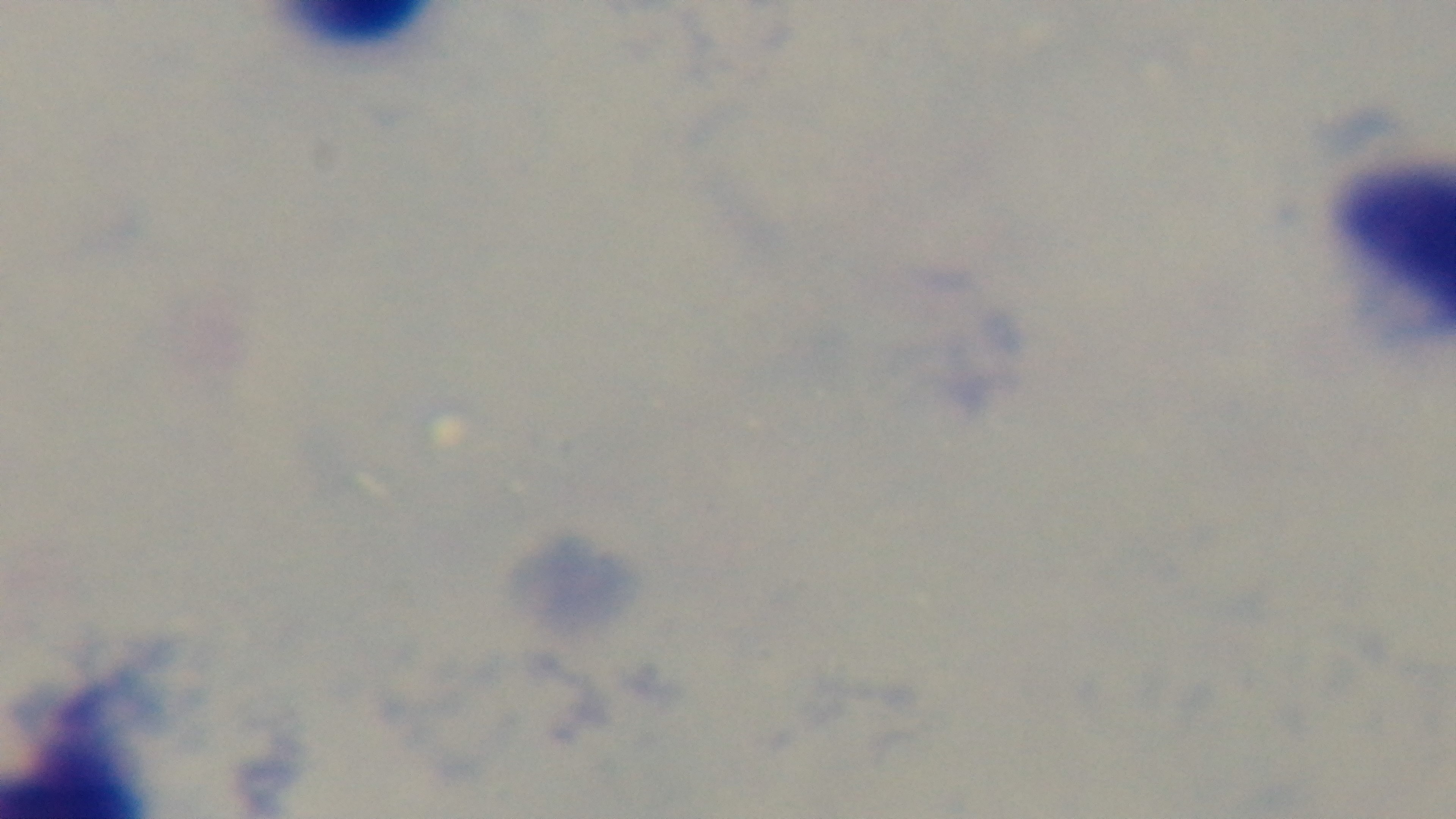

Summary:
  - Malaria status: uninfected
  - Modality: light microscopy
  - Stain: Giemsa
  - Preparation: thick blood film
  - Objective: 100x oil immersion
  - Field of view: single
  - Capture: mounted 4K digital camera